Report the malaria status of this cell.
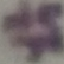
It is uninfected.

Summary:
  - Preparation: thin blood smear
  - Stain: Giemsa
  - Capture: smartphone camera at the microscope eyepiece
  - Image type: cell patch, automatically extracted from a larger field of view and resized to 64 × 64 pixels